Mark where leukocytes are.
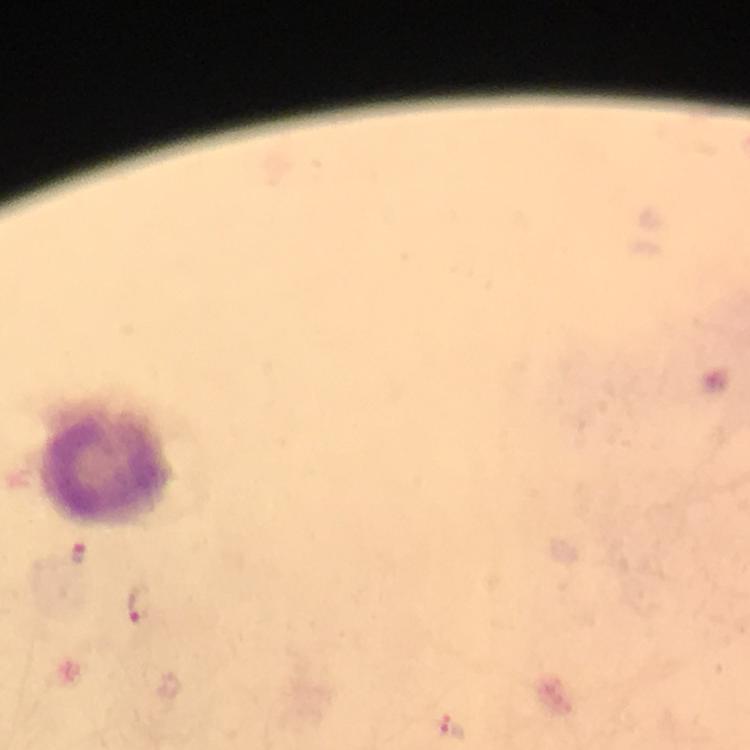

Approximate centers as [x, y] in pixels.
Leukocytes: [110, 473].

Summary:
  - Plasmodium parasite locations: [80, 556], [136, 605], [452, 727]
  - Context: from a malaria diagnostic workup
  - Stain: Giemsa
  - Immersion oil: used
  - Magnification: 100x
  - Cropped from: a single field of view
  - Capture: smartphone photograph through a microscope
  - Preparation: thick blood film
  - Image size: 750×750 pixels